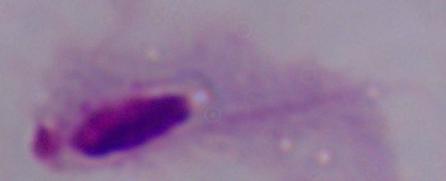
Summary:
  - Modality: photomicrograph
  - Identification: trichomonad
  - Magnification: 1000x